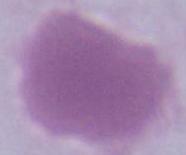 An erythrocyte is shown. Captured at 1000x magnification. Photomicrograph.